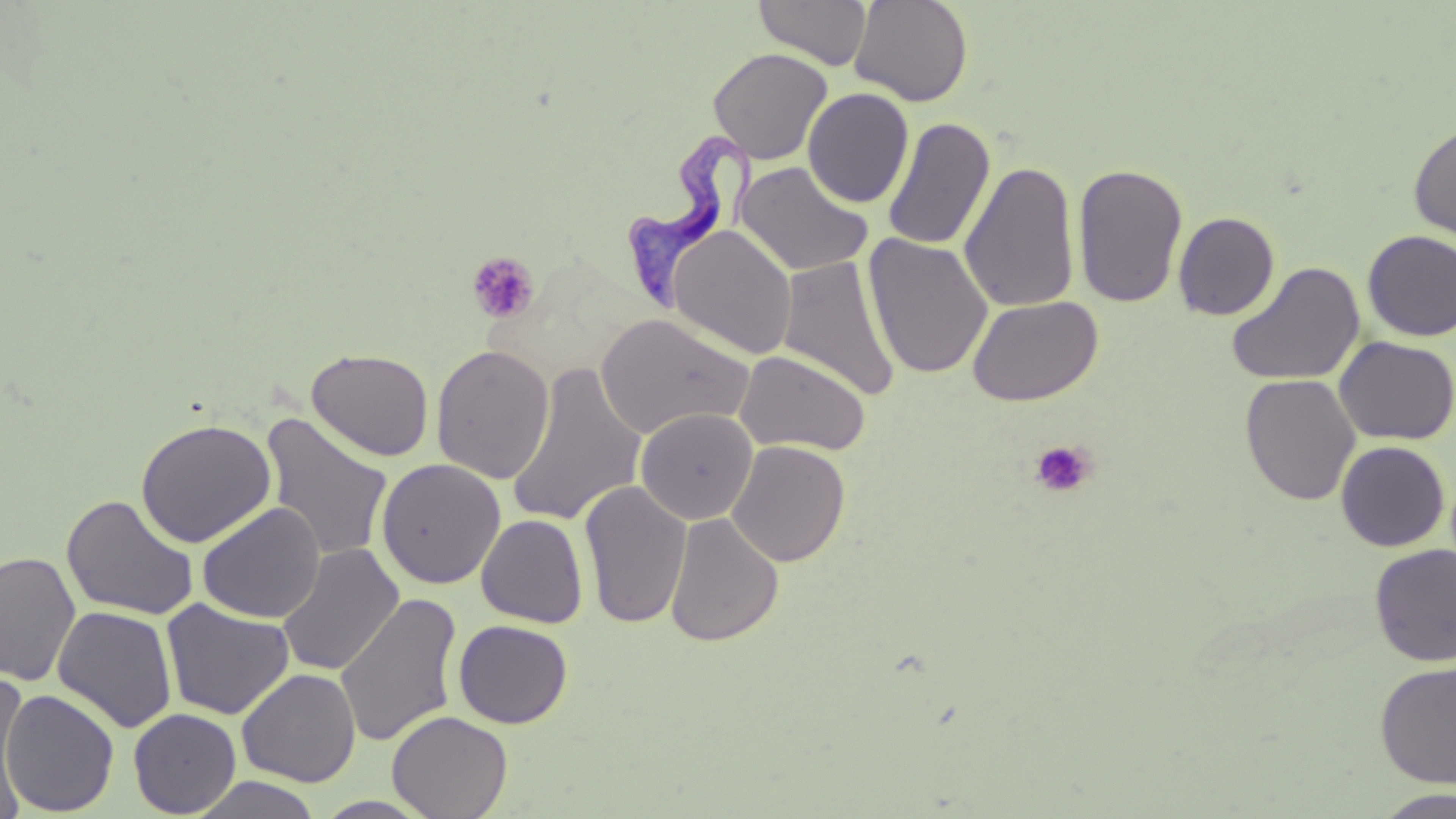
Summary:
  - Coordinate format: approximate bounding boxes as [x1, y1, x2, y2] in pixels
  - Uninfected red blood cell locations: [755, 0, 872, 70], [850, 0, 973, 107], [708, 47, 833, 164], [803, 87, 915, 208], [883, 118, 995, 251], [1408, 118, 1456, 243], [960, 159, 1080, 313], [735, 161, 874, 277], [1072, 162, 1188, 310], [1173, 211, 1279, 320], [668, 225, 798, 359], [1362, 230, 1456, 341], [864, 233, 993, 380], [776, 255, 899, 400], [1225, 260, 1365, 387], [967, 295, 1104, 406], [595, 313, 753, 439], [1335, 336, 1456, 445], [431, 344, 555, 484], [306, 348, 434, 461], [735, 349, 871, 456], [507, 363, 647, 528], [1240, 373, 1360, 506], [635, 408, 759, 525], [260, 412, 395, 563], [135, 418, 276, 548], [727, 440, 851, 567], [1336, 440, 1450, 551], [376, 459, 506, 589], [579, 480, 692, 630], [61, 494, 199, 621], [197, 503, 325, 623], [665, 511, 783, 647], [476, 514, 588, 628], [276, 543, 404, 677], [1369, 544, 1456, 666], [0, 551, 81, 687], [335, 592, 463, 750], [161, 599, 294, 720], [52, 606, 178, 733], [453, 619, 573, 728], [1375, 660, 1456, 787], [237, 668, 361, 787], [0, 674, 32, 817], [1, 688, 120, 816], [128, 708, 242, 818], [387, 710, 513, 819], [189, 775, 324, 819], [1374, 788, 1456, 818], [312, 796, 438, 818]
  - Platelet locations: [466, 252, 540, 324], [1030, 439, 1096, 499]
  - Trypanosoma brucei locations: [627, 125, 761, 314]
  - Slide-level diagnosis: Trypanosoma brucei
  - Field of view: single
  - Magnification: 1000x
  - Stain: May-Grünwald-Giemsa
  - Image size: 1456×819 pixels
  - Modality: optical microscopy
  - Preparation: thin blood smear